Locate and identify every blood parasite.
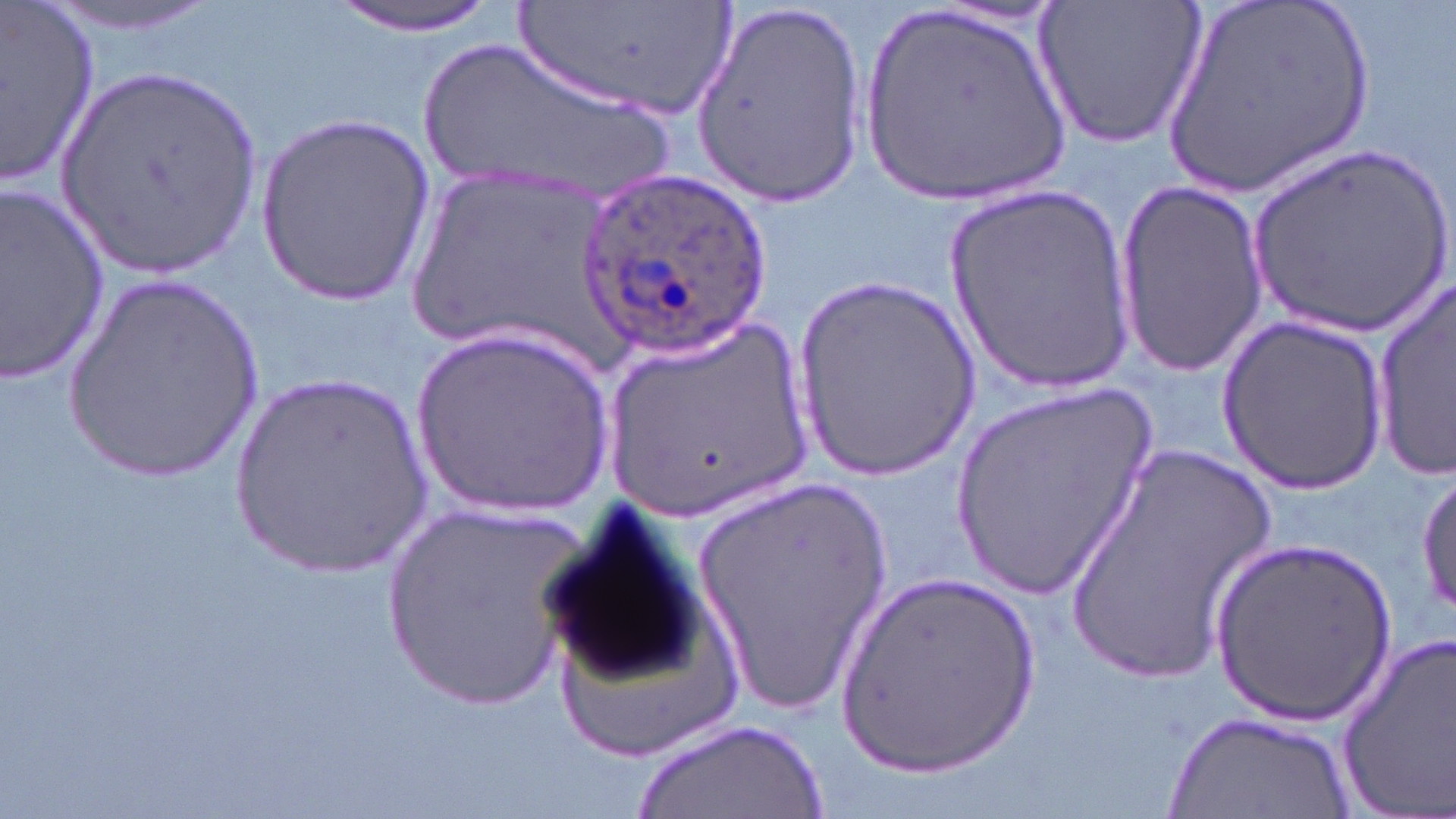
Approximate bounding boxes as (x1, y1, x2, y2) in pixels.
Plasmodium ovale-infected red blood cells: (579, 165, 770, 361).
No Plasmodium falciparum, Plasmodium malariae, Plasmodium vivax, Babesia divergens, or Trypanosoma brucei observed.

Summary:
  - Uninfected red blood cell locations: (40, 0, 229, 38), (326, 0, 507, 36), (513, 0, 742, 118), (1034, 0, 1208, 151), (1154, 0, 1382, 203), (0, 1, 102, 189), (863, 1, 1073, 209), (690, 2, 867, 204), (409, 35, 686, 203), (58, 67, 265, 280), (256, 115, 433, 306), (1246, 144, 1453, 345), (399, 163, 618, 368), (1110, 177, 1270, 382), (0, 181, 110, 384), (943, 184, 1138, 395), (793, 274, 982, 483), (59, 276, 267, 484), (1371, 276, 1456, 476), (597, 311, 821, 520), (1216, 316, 1394, 491), (413, 323, 617, 526), (227, 372, 437, 579), (951, 383, 1160, 598), (1060, 438, 1283, 683), (1415, 471, 1456, 623), (692, 478, 892, 714), (534, 493, 716, 697), (379, 504, 594, 714), (1210, 541, 1396, 725), (833, 570, 1046, 779), (1335, 630, 1456, 816), (1165, 711, 1356, 818), (637, 718, 826, 819)
  - Slide-level diagnosis: Plasmodium ovale
  - Modality: optical microscopy
  - Field of view: single
  - Stain: May-Grünwald-Giemsa
  - Magnification: 1000x
  - Image size: 1456×819 pixels
  - Preparation: thin blood film